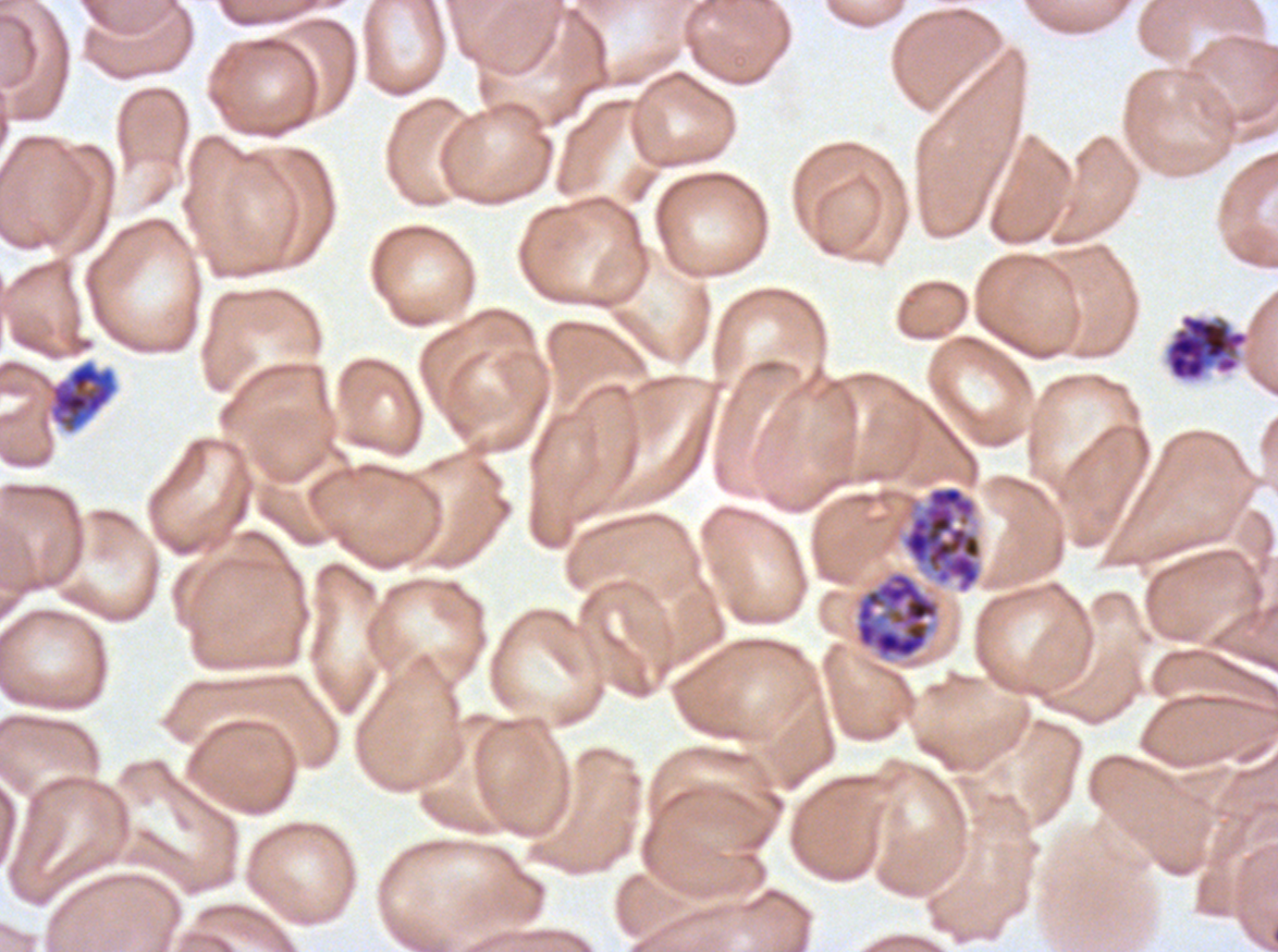
Approximate bounding rectangles given as corner coordinates in pixels from the top-left. Early schizont locations: (x1=50, y1=361, x2=116, y2=433). Segmenter locations: (x1=1164, y1=312, x2=1250, y2=382). Late schizont locations: (x1=900, y1=484, x2=983, y2=594), (x1=854, y1=570, x2=940, y2=660). Ex-vivo P. falciparum culture from a patient in The Gambia, grown for 24 to 48 hours. Thin blood film. Life-cycle stages observed: early schizont, late schizont, segmenter. Image is 1278×952 pixels. Giemsa stain. A sub-image separated from a larger composite.